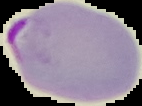 From a thin blood smear. Image is 142×106 pixels. Segmented cell region on a black background. Malaria status: parasitized.